Classify this cell by malaria status.
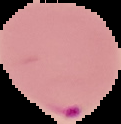

It is parasitized.

Image is 121×124 pixels. From a thin blood film. Cell region segmented out of the field of view; the surrounding area is masked to black.